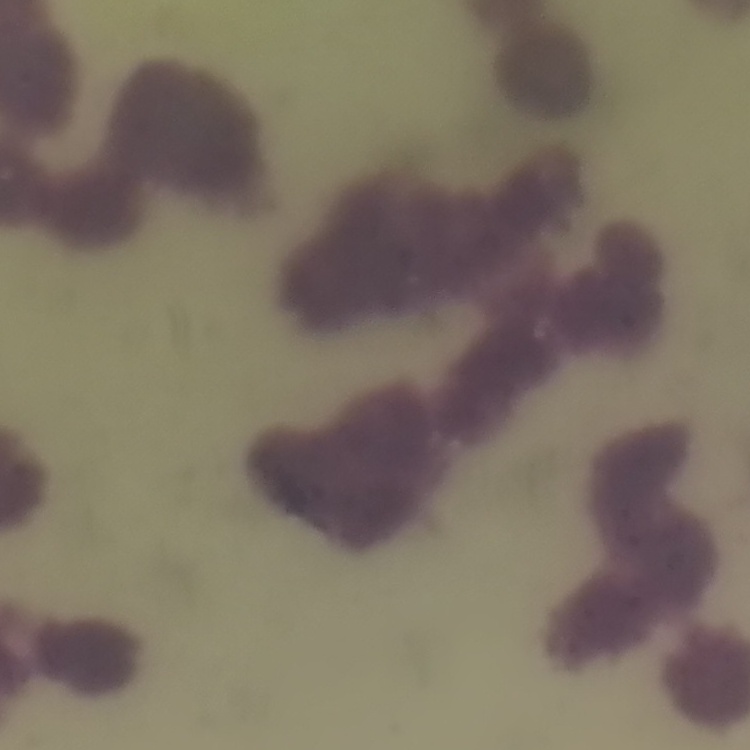

The red blood cells show rouleaux formation. One tile cut from a larger photomicrograph. Thin blood film. Field's or Giemsa stain.